Report the malaria status of this cell.
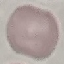

Uninfected.

Summary:
  - Stain: Giemsa
  - Image type: cell patch, automatically extracted from a larger field of view and resized to 64 × 64 pixels
  - Preparation: thin blood film
  - Capture: smartphone through the microscope eyepiece